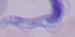

Photomicrograph. A trypanosome is shown. Captured at 1000x magnification.